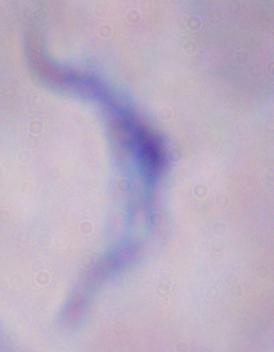

identification = trypanosome
magnification = 1000x
modality = photomicrograph